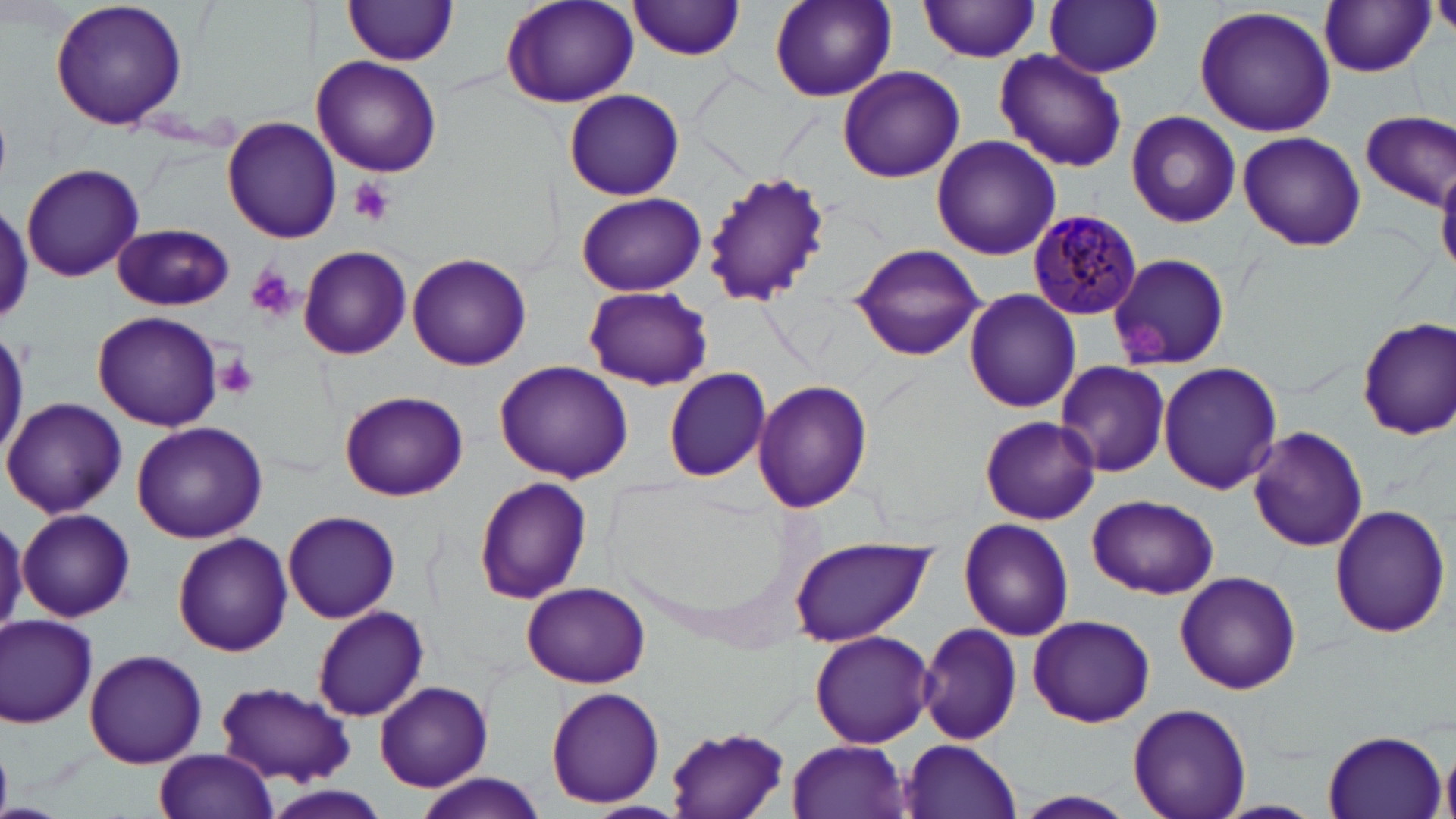
Plasmodium malariae-infected red blood cell locations = approximate bounding boxes as (x1, y1, x2, y2) in pixels: (1029, 209, 1144, 321)
slide-level diagnosis = Plasmodium malariae
image size = 1456×819 pixels
modality = light microscopy
preparation = thin blood film
stain = May-Grünwald-Giemsa
magnification = 1000x
platelet locations = approximate bounding boxes as (x1, y1, x2, y2) in pixels: (349, 178, 395, 226), (242, 265, 298, 323), (1127, 323, 1174, 359), (215, 353, 260, 398)
field of view = one of a larger specimen
uninfected red blood cell locations = approximate bounding boxes as (x1, y1, x2, y2) in pixels: (48, 0, 189, 133), (344, 0, 458, 67), (630, 0, 746, 60), (768, 0, 898, 105), (919, 1, 1044, 63), (1045, 1, 1164, 76), (502, 2, 640, 109), (1319, 2, 1435, 76), (1193, 5, 1338, 139), (995, 46, 1130, 173), (311, 56, 441, 177), (836, 64, 965, 184), (565, 89, 684, 201), (1126, 109, 1242, 228), (1359, 111, 1455, 210), (223, 116, 341, 244), (1237, 132, 1365, 251), (931, 136, 1060, 259), (21, 163, 144, 281), (1437, 165, 1456, 277), (703, 172, 832, 304), (576, 192, 705, 295), (0, 201, 32, 330), (113, 225, 235, 311), (849, 242, 986, 361), (299, 247, 412, 360), (1108, 252, 1231, 370), (408, 254, 530, 370), (583, 285, 713, 390), (963, 287, 1082, 414), (91, 309, 224, 431), (1356, 318, 1455, 438), (1157, 360, 1283, 495), (1052, 361, 1171, 478), (494, 362, 632, 481), (663, 366, 772, 483), (752, 381, 873, 514), (340, 390, 469, 499), (3, 397, 126, 518), (980, 416, 1100, 525), (132, 422, 267, 543), (1247, 425, 1369, 551), (474, 477, 593, 604), (1088, 494, 1218, 599), (1329, 504, 1451, 636), (17, 508, 136, 622), (283, 511, 399, 621), (0, 514, 28, 635), (959, 519, 1074, 641), (173, 533, 293, 656), (789, 535, 939, 647), (1174, 570, 1301, 694), (522, 582, 651, 689), (313, 606, 429, 721), (1, 613, 99, 729), (1026, 614, 1155, 728), (917, 622, 1023, 746), (810, 629, 934, 749), (83, 648, 208, 767), (374, 681, 493, 792), (216, 682, 355, 784), (546, 686, 666, 809), (1128, 702, 1251, 819), (664, 728, 792, 818), (1322, 730, 1447, 819), (787, 739, 912, 818), (899, 739, 1022, 818), (1440, 746, 1456, 819), (154, 748, 280, 819), (415, 773, 548, 819), (262, 785, 391, 819), (1007, 791, 1140, 819), (1211, 800, 1325, 818)